Locate every malaria parasite.
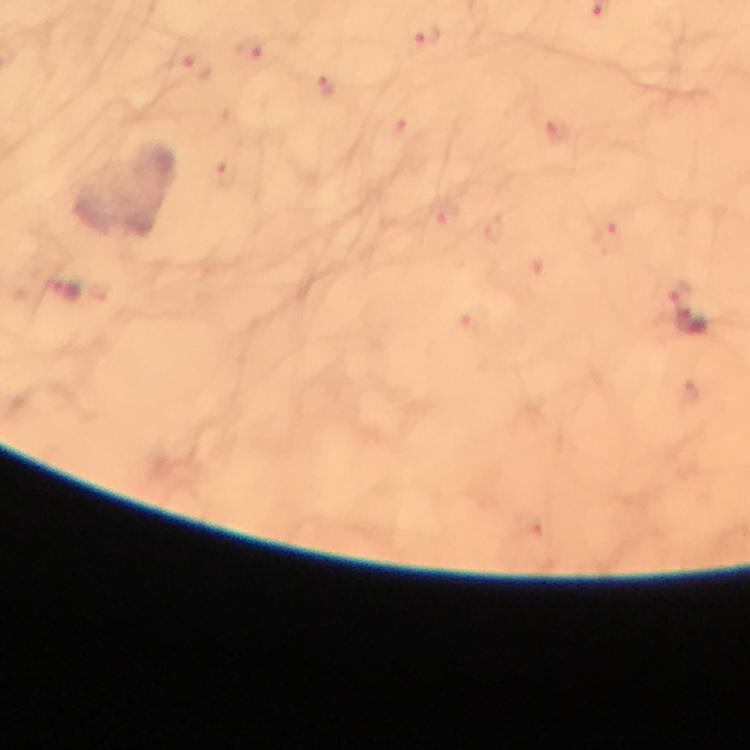
Approximate centers as {x, y} in pixels.
Malaria parasites: {426, 35}, {246, 49}, {197, 67}, {323, 86}, {559, 131}, {223, 174}, {609, 237}, {68, 291}, {679, 291}.

Summary:
  - Capture: smartphone camera through the microscope
  - Stain: Giemsa
  - Context: from a malaria diagnostic workup
  - Cropped from: a single field of view
  - Image size: 750×750 pixels
  - Preparation: thick smear
  - Immersion oil: used
  - Magnification: 100x